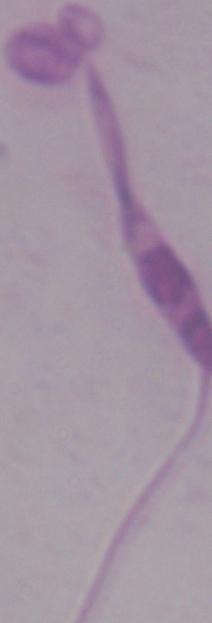
Captured at 1000x magnification. Photomicrograph. A Leishmania parasite is seen.